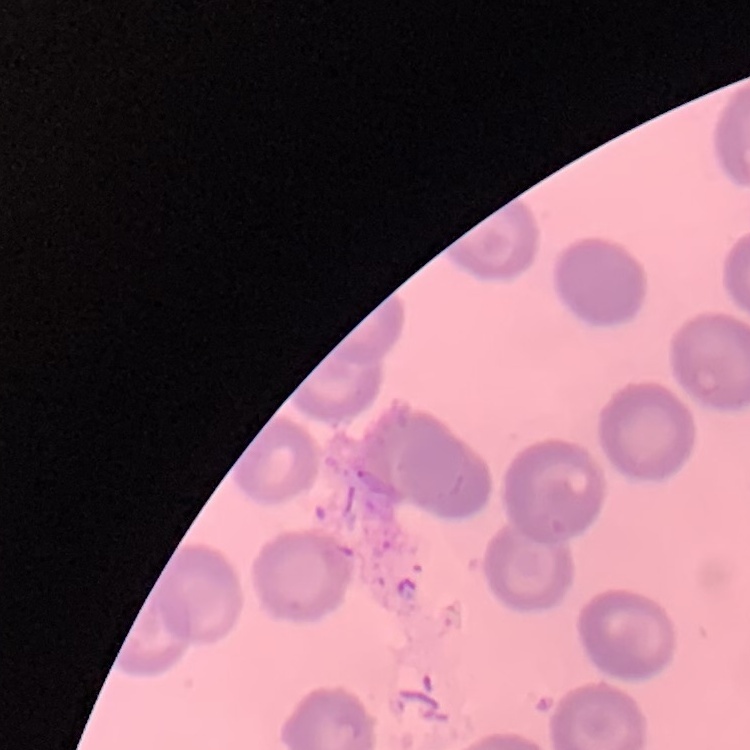
erythrocyte morphology = no rouleaux formation
image type = one tile cut from a larger photomicrograph
preparation = thin blood smear
stain = Field's or Giemsa